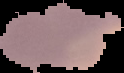

Cell region segmented out of the field of view; the surrounding area is masked to black. Image is 124×73 pixels. From a thin blood smear. Result: malaria parasites identified.